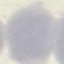
Result: no malaria parasites seen. Giemsa stain. Automatically extracted cell patch, resized to 64 × 64 pixels. Thin smear of blood. Acquired by smartphone through the microscope eyepiece.